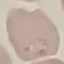

Result: malaria parasites identified. Acquired by smartphone through the microscope eyepiece. Thin smear of blood. Cell patch, automatically extracted from a larger field of view and resized to 64 × 64 pixels. Giemsa stain.